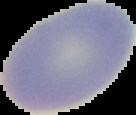 Segmented cell region on a black background. From a thin blood smear. Result: no malaria parasites seen. Image is 136×115 pixels.